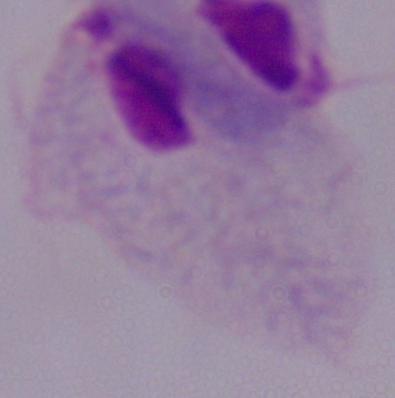
identification = trichomonad
modality = micrograph
magnification = 1000x